State which parasite is depicted.
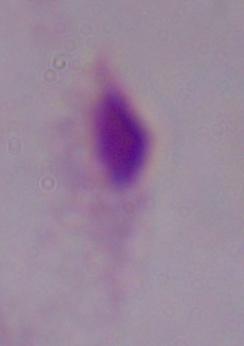

A trichomonad.

Summary:
  - Magnification: 1000x
  - Modality: micrograph